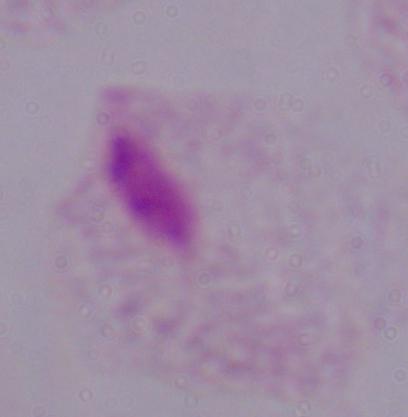 1000x magnification. A trichomonad is shown. Micrograph.